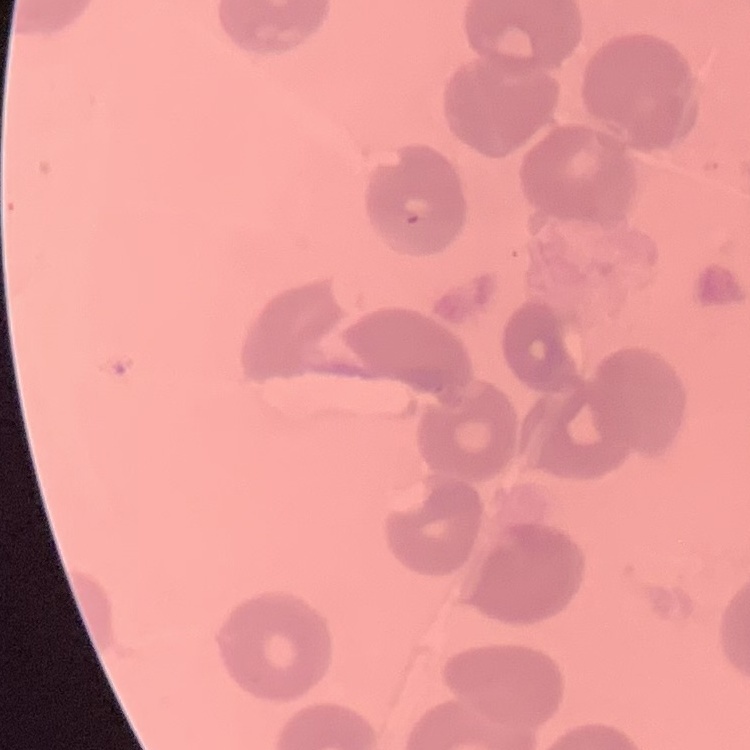
The red blood cells exhibit no rouleaux formation. One tile cut from a larger photomicrograph. Thin blood film. Field's or Giemsa stain.